Classify this cell by malaria status.
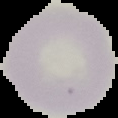

It is uninfected.

Summary:
  - Preparation: thin blood film
  - Image size: 118×118 pixels
  - Image type: cell region segmented out of the field of view; surrounding area masked to black